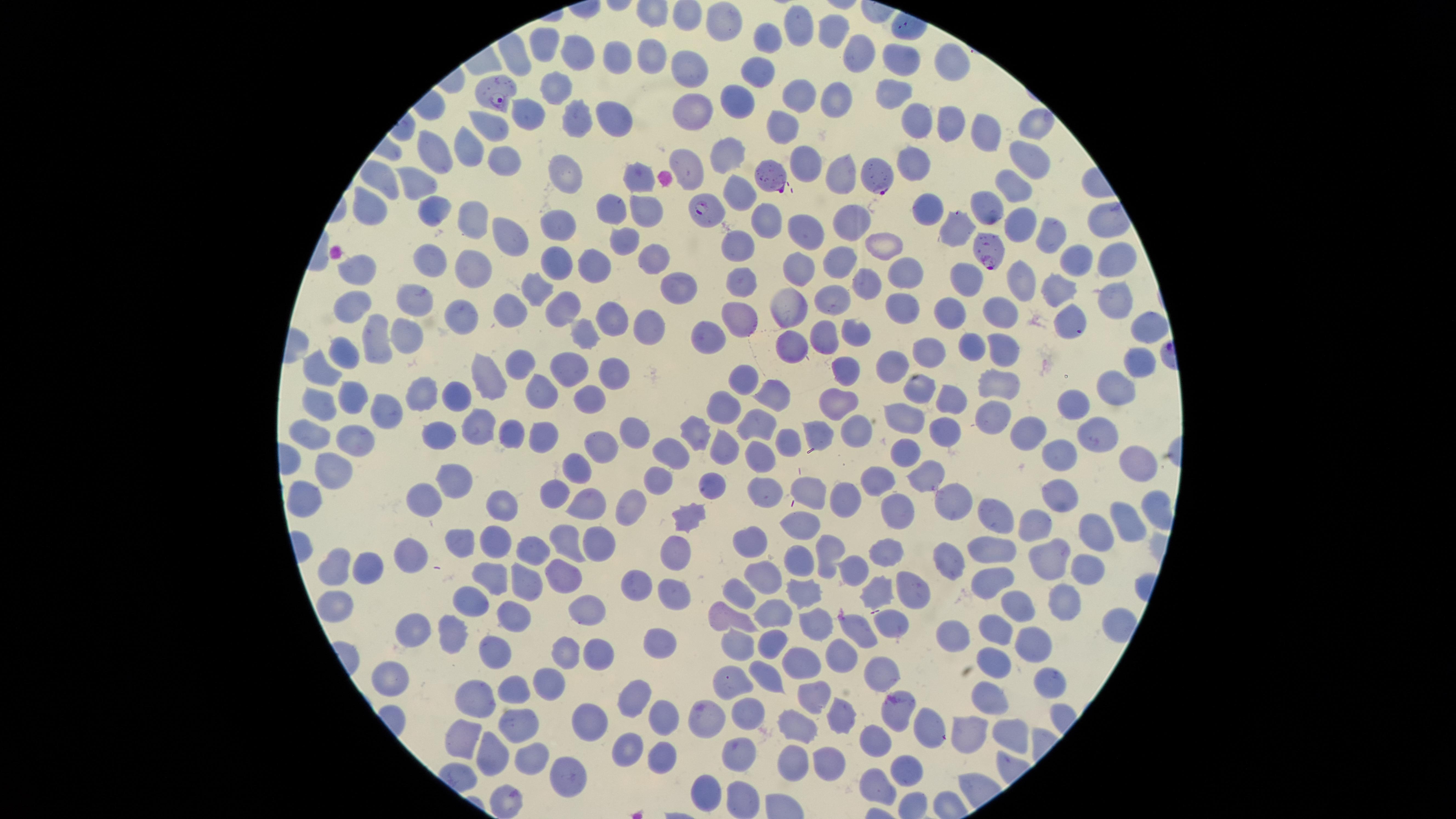

presence = malaria parasites identified
species = Plasmodium falciparum
uninfected red blood cells = approximate marker points as [x, y] in pixels: [718, 18], [801, 25], [836, 31], [770, 33], [538, 46], [581, 53], [651, 53], [858, 56], [898, 58], [614, 62], [949, 62], [683, 66], [758, 72], [563, 83], [896, 90], [800, 94], [836, 99], [739, 101], [693, 111], [526, 115], [611, 119], [578, 120], [916, 121], [1029, 122], [947, 124], [783, 125], [487, 130], [979, 131], [735, 148], [435, 152], [1027, 154], [461, 155], [688, 161], [806, 162], [502, 163], [915, 167], [572, 172], [631, 174], [840, 174], [416, 184], [1012, 189], [742, 194], [983, 206], [377, 208], [611, 208], [435, 209], [928, 210], [642, 212], [470, 214], [764, 215], [847, 219], [1016, 221], [563, 226], [804, 228], [957, 229], [504, 231], [621, 237], [1042, 237], [742, 241], [884, 246], [557, 255], [648, 256], [1118, 258], [839, 259], [1070, 260], [433, 261], [593, 261], [802, 265], [474, 270], [905, 270], [360, 274], [963, 276], [740, 277], [863, 279], [675, 281], [1020, 281], [540, 287], [1058, 288], [407, 293], [1110, 297], [834, 301], [353, 302], [464, 306], [565, 306], [790, 307], [899, 308], [996, 310], [608, 314], [742, 315], [1074, 317], [952, 319], [647, 323], [1144, 324], [714, 326], [584, 327], [856, 331], [409, 332], [375, 336], [786, 341], [821, 342], [971, 345], [1002, 346], [930, 350], [348, 353], [518, 362], [893, 362], [573, 365], [1138, 365], [321, 368], [489, 368], [608, 371], [837, 372], [747, 377], [1007, 381], [420, 387], [922, 388], [1113, 388], [773, 390], [539, 394], [1071, 395], [586, 396], [350, 397], [451, 397], [947, 398], [321, 399], [838, 402], [725, 406], [381, 410], [986, 415], [911, 419], [757, 424], [699, 428], [475, 430], [854, 430], [942, 430], [1094, 430], [1030, 433], [513, 435], [541, 435], [311, 436], [638, 436], [820, 438], [353, 439], [788, 440], [440, 441], [724, 444], [603, 446], [675, 451], [758, 452], [908, 454], [1059, 454], [1132, 464], [336, 468], [582, 468], [922, 474], [879, 476], [457, 479], [661, 482], [710, 482], [808, 485], [754, 489], [558, 493], [953, 493], [307, 496], [428, 498], [1060, 498], [588, 501], [627, 501], [842, 501], [498, 504], [900, 508], [997, 510], [685, 518], [1125, 519], [1039, 523], [804, 529], [1092, 530], [744, 537], [465, 539], [491, 542], [566, 543], [597, 543], [989, 545], [678, 548], [826, 549], [891, 551], [528, 553], [1050, 555], [943, 556], [414, 557], [336, 565], [802, 565], [1083, 569], [852, 570], [561, 572], [988, 574], [525, 576], [368, 577], [753, 577], [486, 578], [637, 582], [917, 585], [882, 586], [675, 590], [735, 593], [807, 595], [469, 597], [1062, 602], [337, 604], [1023, 609], [588, 612], [721, 612], [774, 616], [518, 617], [813, 621], [891, 626], [856, 627], [999, 629], [415, 630], [454, 630], [954, 637], [769, 644], [741, 645], [1033, 645], [661, 647], [567, 648], [842, 649], [495, 650], [595, 651], [997, 660], [803, 661], [880, 667], [392, 671], [768, 679], [1050, 679], [550, 682], [515, 684], [726, 685], [641, 691], [815, 695], [479, 697], [985, 705], [845, 706], [894, 711], [712, 715], [657, 716], [590, 718], [749, 718], [798, 720], [518, 721], [926, 728], [1008, 730], [964, 736], [466, 738], [882, 740], [626, 745], [531, 754], [741, 754], [488, 755], [660, 758], [826, 759], [793, 764], [571, 769], [905, 770], [709, 787], [876, 789], [507, 797], [741, 800]
visible region = circular
image size = 1456×819 pixels
capture = smartphone photograph through the microscope eyepiece
preparation = thin blood smear
field of view = single
stain = Giemsa
parasitized red blood cells = approximate marker points as [x, y] in pixels: [497, 95], [881, 175], [773, 178], [708, 206], [989, 250]